Point out each leukocyte.
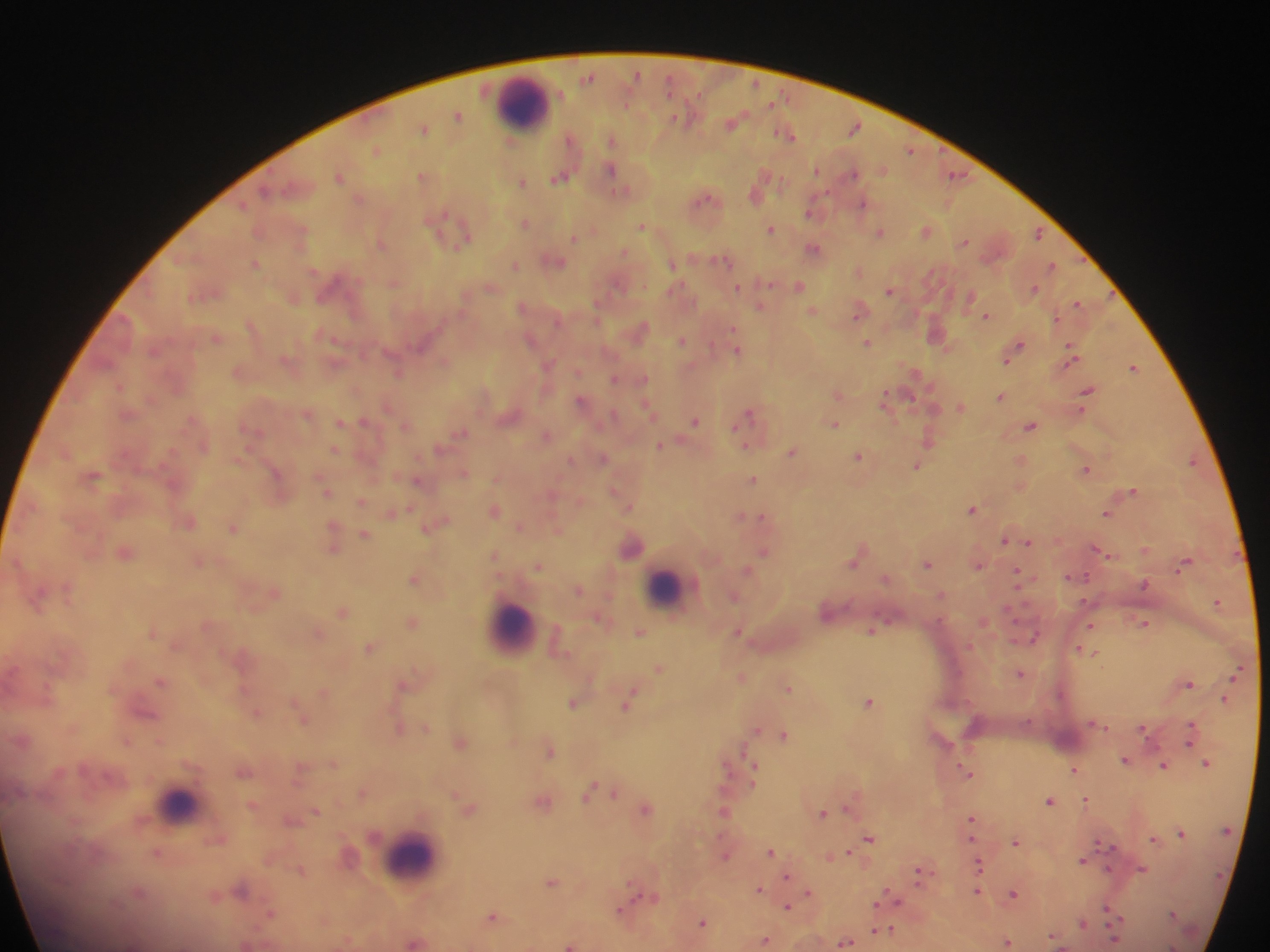

Approximate centers as [x, y] in pixels.
Leukocytes: [524, 103], [667, 586], [511, 628], [180, 803], [410, 857].

field of view = single
image size = 1270×952 pixels
capture = mobile-phone photograph through a microscope
country = Ghana
malaria parasite locations = approximate centers as [x, y] in pixels: [636, 73], [588, 77], [669, 84], [458, 116], [733, 122], [855, 128], [423, 129], [792, 136], [612, 140], [377, 150], [911, 151], [611, 169], [818, 171], [852, 174], [957, 175], [340, 176], [422, 177], [560, 178], [523, 183], [757, 191], [704, 199], [863, 205], [809, 211], [525, 224], [642, 225], [770, 229], [926, 231], [302, 232], [881, 232], [1038, 234], [574, 238], [466, 239], [964, 241], [380, 243], [814, 248], [624, 252], [722, 260], [556, 262], [254, 263], [673, 264], [515, 265], [1052, 266], [738, 287], [799, 287], [1034, 288], [890, 291], [969, 297], [1079, 304], [522, 306], [761, 306], [812, 311], [858, 311], [986, 316], [642, 330], [215, 337], [682, 341], [423, 342], [866, 343], [1018, 346], [737, 350], [1071, 354], [1009, 356], [549, 364], [396, 366], [1134, 367], [578, 372], [614, 379], [644, 379], [119, 386], [1088, 391], [1000, 396], [910, 398], [886, 399], [581, 401], [646, 406], [961, 406], [388, 407], [749, 413], [308, 414], [613, 415], [365, 421], [696, 421], [341, 422], [834, 424], [405, 426], [1029, 426], [462, 433], [546, 435], [929, 439], [659, 445], [743, 445], [335, 450], [792, 451], [858, 456], [603, 458], [570, 460], [1192, 462], [917, 466], [1086, 469], [276, 473], [464, 473], [92, 476], [753, 479], [418, 481], [327, 491], [1134, 491], [360, 502], [628, 508], [972, 509], [494, 511], [392, 512], [1107, 514], [753, 515], [740, 516], [762, 516], [189, 523], [436, 524], [519, 527], [233, 529], [365, 535], [1004, 539], [1028, 542], [332, 543], [632, 547], [1098, 550], [1144, 550], [764, 551], [125, 553], [853, 561], [198, 562], [1184, 563], [928, 564], [979, 565], [539, 566], [1017, 573], [1084, 577], [413, 579], [885, 579], [1145, 584], [579, 590], [734, 596], [1217, 602], [343, 612], [412, 623], [1145, 623], [1090, 626], [872, 630], [640, 632], [737, 632], [318, 633], [1036, 636], [371, 648], [1087, 651], [1093, 654], [659, 669], [1020, 673], [741, 677], [160, 681], [1189, 684], [402, 686], [788, 687], [1225, 698], [629, 700], [573, 702], [869, 702], [256, 712], [301, 718], [426, 728], [398, 729], [1144, 729], [755, 730], [785, 734], [1190, 735], [127, 741], [159, 742], [460, 743], [548, 750], [1125, 761], [1207, 764], [1164, 766], [1074, 770], [754, 771], [965, 771], [589, 790], [363, 792], [613, 793], [1087, 800], [1048, 801], [543, 803], [849, 806], [645, 809], [469, 810], [317, 811], [724, 813], [823, 813], [970, 820], [1181, 832], [1153, 838], [869, 839], [1016, 842], [770, 851], [157, 853], [846, 853], [725, 855], [1082, 860], [978, 865], [301, 869], [1142, 869], [918, 873], [787, 876], [551, 882], [759, 889], [242, 891], [977, 891], [809, 892], [1013, 893], [642, 896], [890, 897], [786, 907], [621, 911], [1109, 912], [1173, 913], [269, 915], [492, 917], [702, 922], [1083, 923], [889, 930], [765, 940], [1007, 942], [415, 943], [845, 943], [246, 945], [569, 945]
preparation = thick blood film